Name the parasite shown.
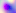

This is Toxoplasma gondii.

Summary:
  - Modality: micrograph
  - Magnification: 400x